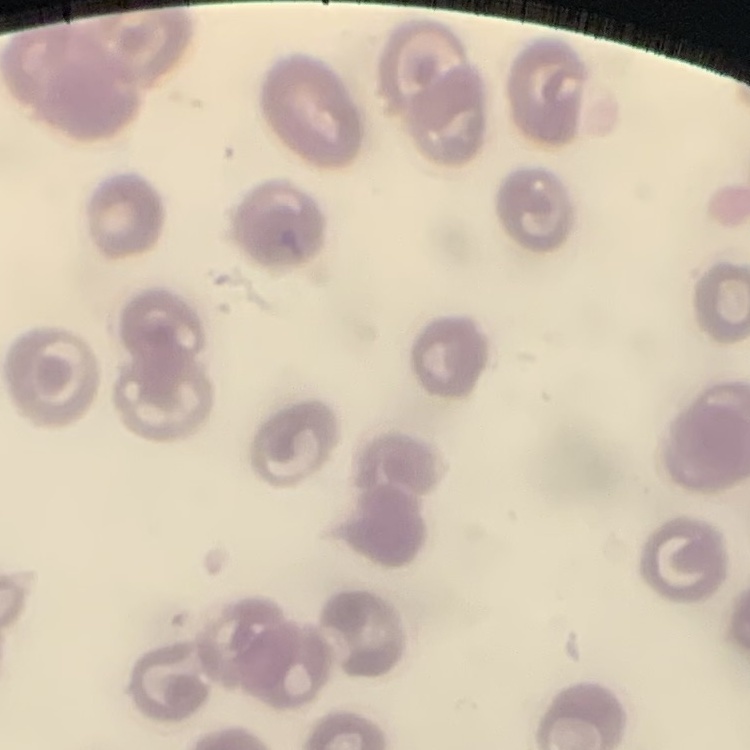
{
  "erythrocyte_morphology": "no rouleaux formation",
  "image_type": "square crop of a larger photomicrograph",
  "preparation": "thin peripheral smear",
  "stain": "Field's or Giemsa"
}